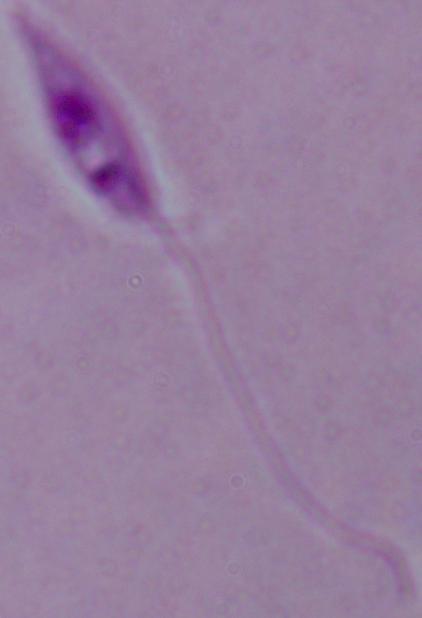
{
  "magnification": "1000x",
  "modality": "photomicrograph",
  "identification": "Leishmania"
}